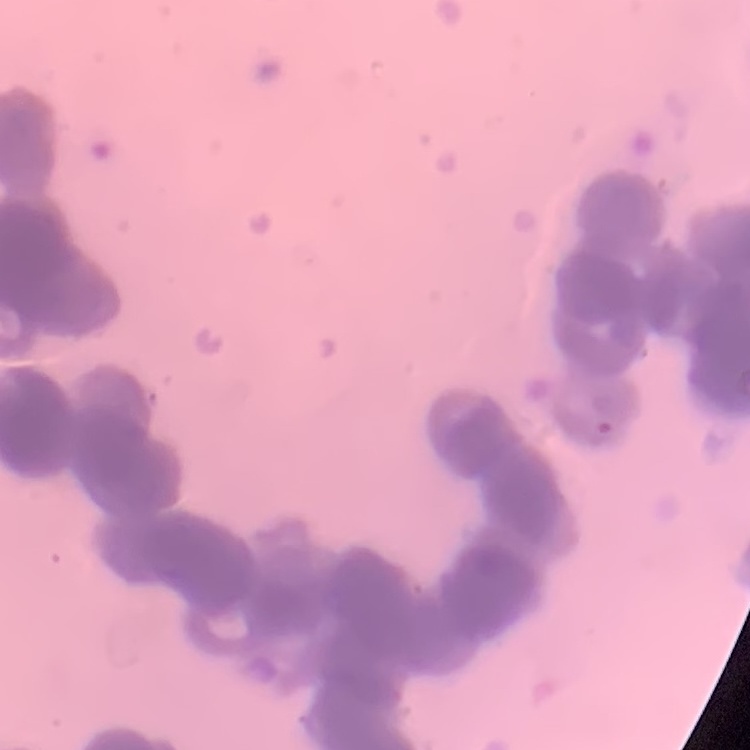

The red blood cells exhibit rouleaux formation. Thin peripheral smear. Field's or Giemsa stain. Square crop of a larger photomicrograph.